Comment on the morphology of the red blood cells.
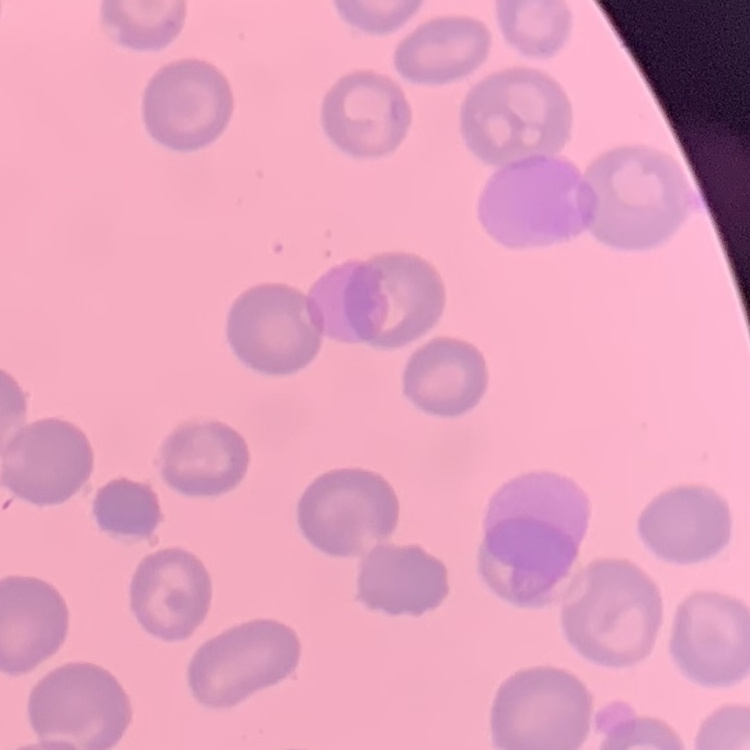

No rouleaux formation.

Summary:
  - Stain: Field's or Giemsa
  - Image type: square crop of a larger photomicrograph
  - Preparation: thin blood film